Identify the parasite.
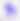
This is Toxoplasma gondii.

magnification = 400x
modality = micrograph